State which parasite is depicted.
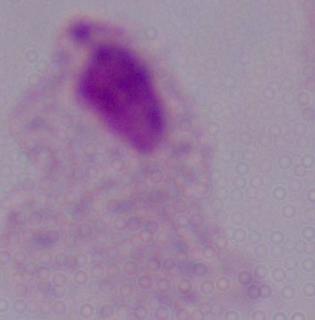
A trichomonad.

{
  "magnification": "1000x",
  "modality": "photomicrograph"
}